Assess this cell for malaria.
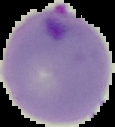
Parasitized.

Summary:
  - Image size: 115×127 pixels
  - Image type: segmented cell region with the area outside set to black
  - Preparation: thin blood smear